Assess the morphology of the erythrocytes.
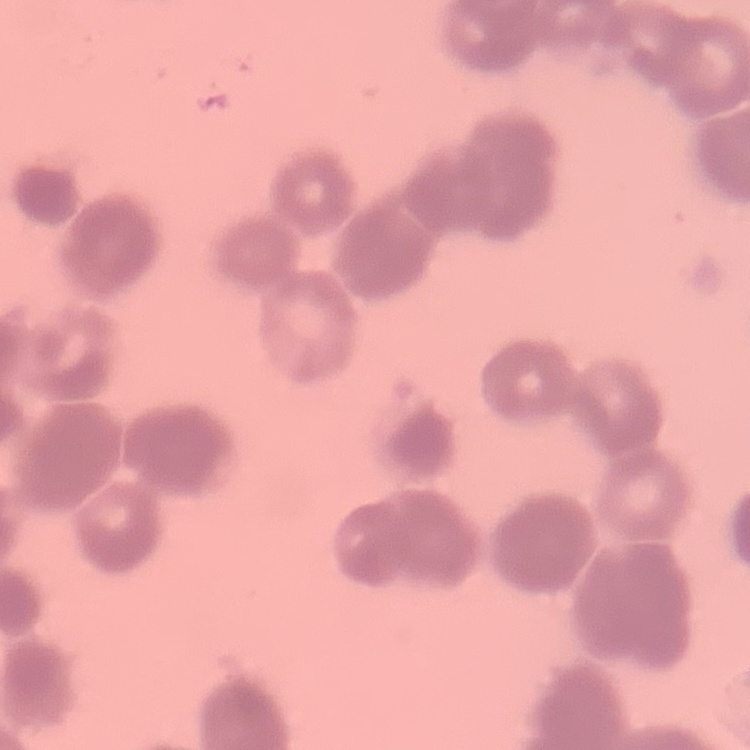

They show rouleaux formation.

Summary:
  - Stain: Field's or Giemsa
  - Preparation: thin blood smear
  - Image type: one tile cut from a larger photomicrograph